Report the malaria status of this cell.
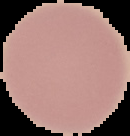

Uninfected.

The area outside the segmented cell region is set to black. From a thin blood smear. Image is 130×136 pixels.